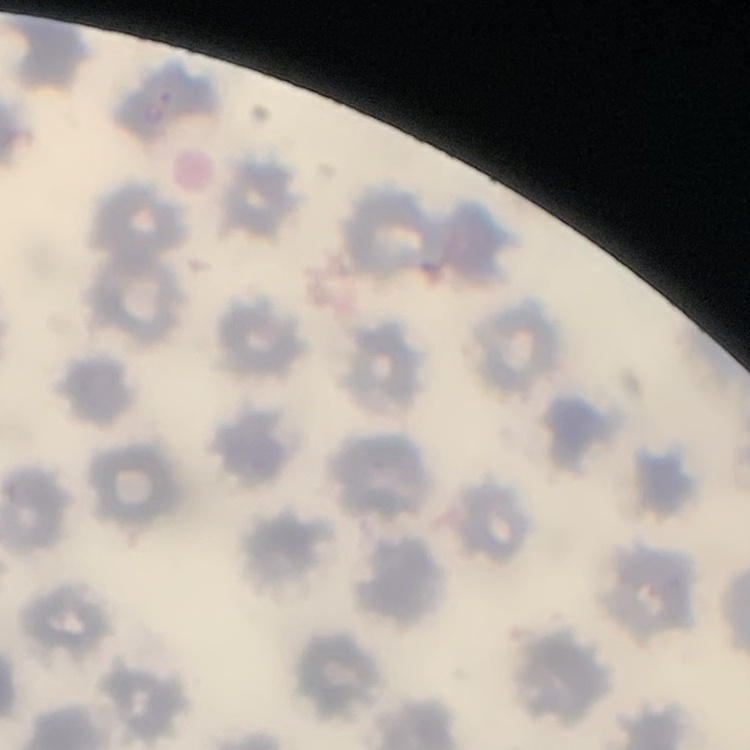

Summary:
  - Red blood cell morphology: no rouleaux formation
  - Stain: Field's or Giemsa
  - Image type: square crop of a larger photomicrograph
  - Preparation: thin peripheral smear